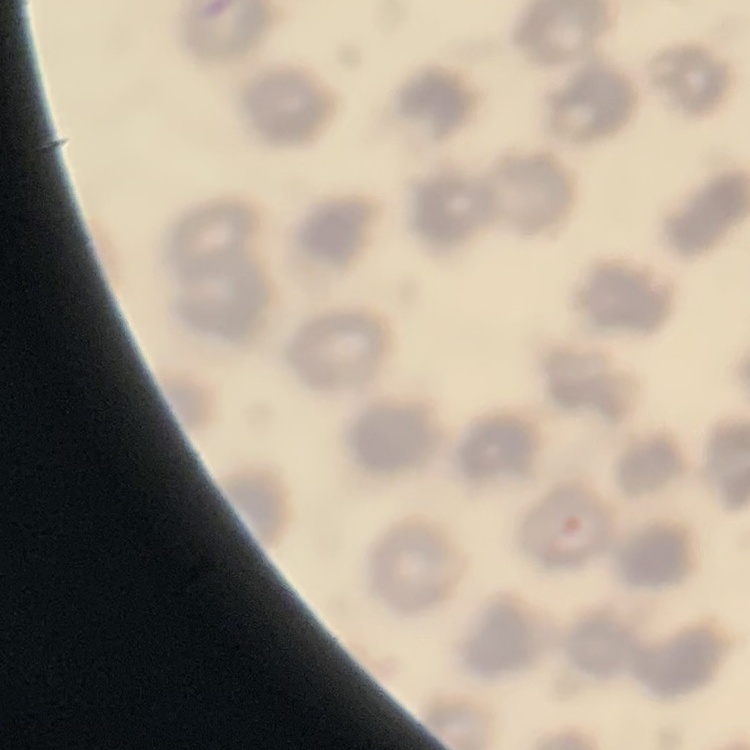
red blood cell morphology = no rouleaux formation
stain = Field's or Giemsa
preparation = thin blood smear
image type = square crop of a larger photomicrograph